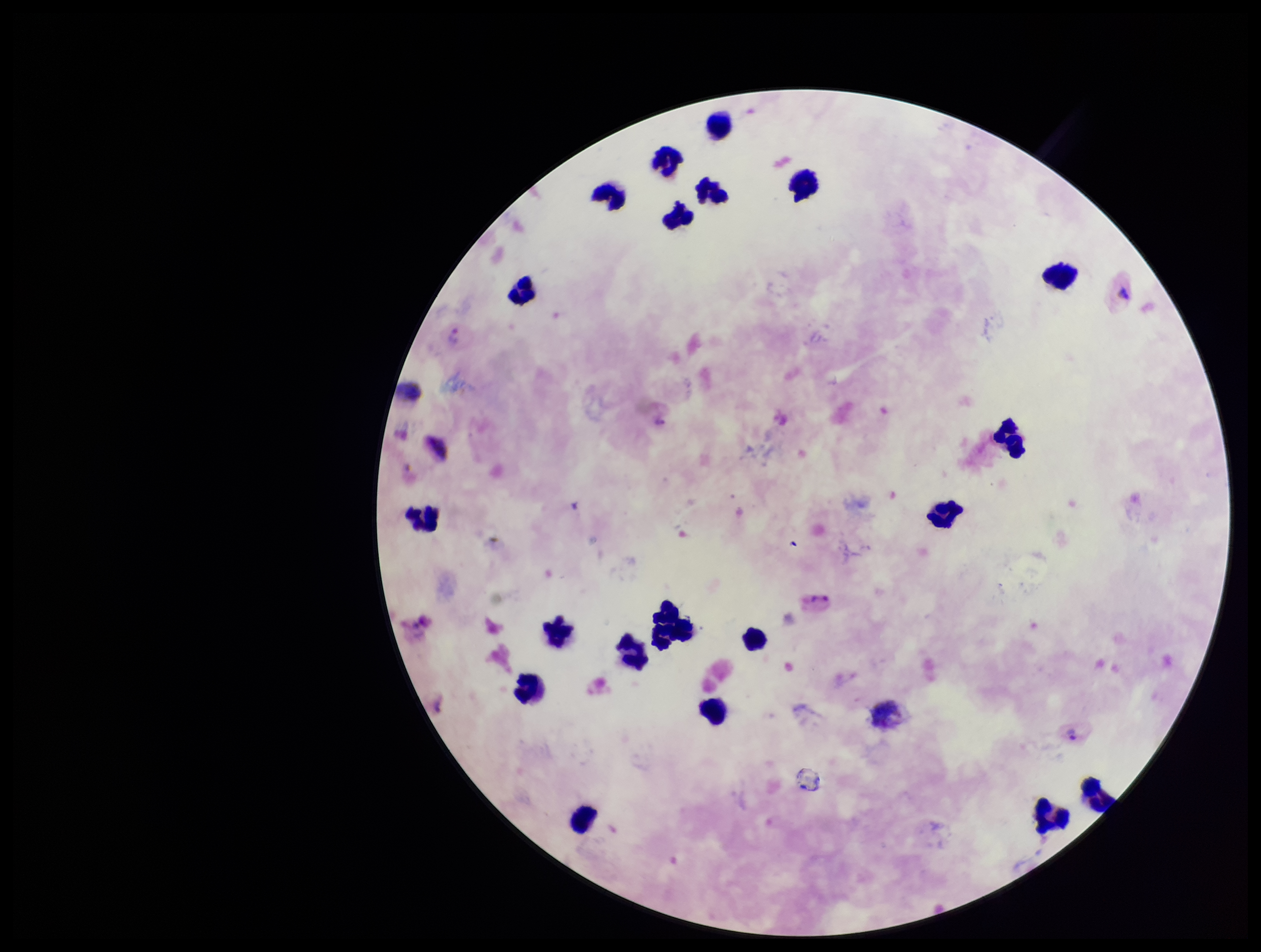
Summary:
  - Stain: Giemsa
  - Image size: 1261×952 pixels
  - Preparation: thick
  - Capture: smartphone photograph through the microscope eyepiece
  - Parasite count: 3
  - Species reported for this patient: Plasmodium vivax
  - Leukocyte count: 20
  - Patient malaria status: positive
  - Plasmodium parasites: detected
  - Field of view: one from this slide